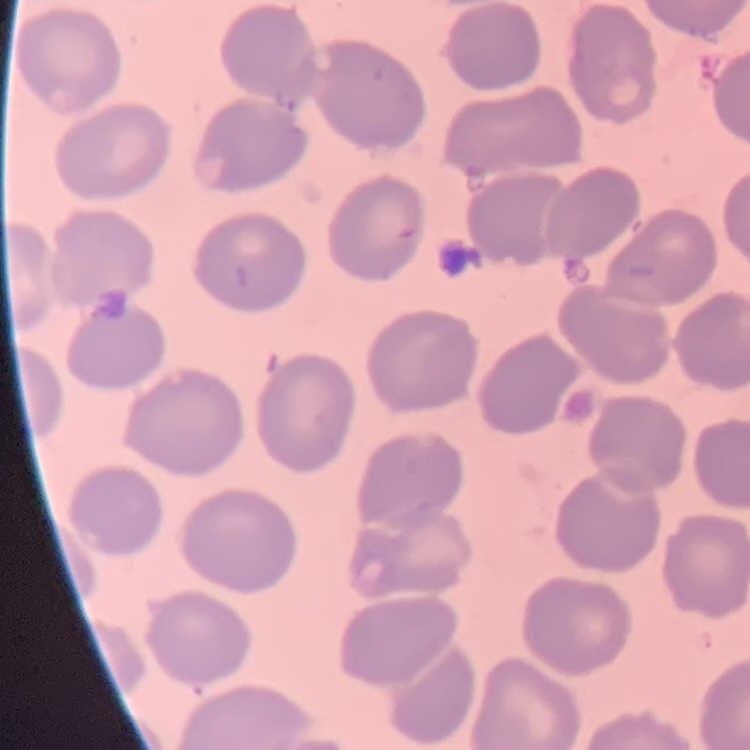

The erythrocytes show no rouleaux formation. Thin peripheral smear. One tile cut from a larger photomicrograph. Field's or Giemsa stain.